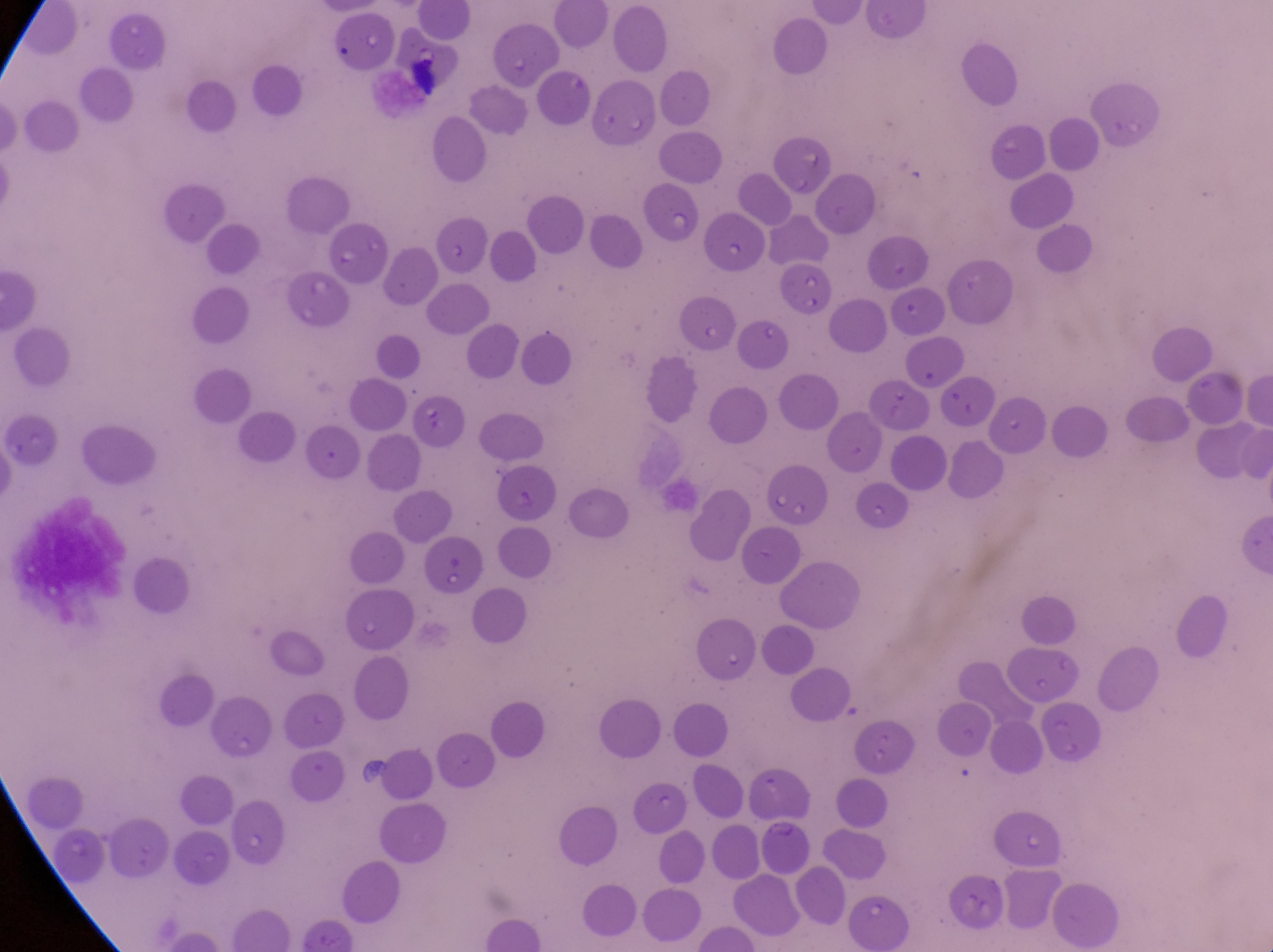
{
  "preparation": "thin blood smear",
  "capture": "smartphone photograph through the eyepiece of an Olympus CX-23 microscope",
  "parasitised_red_blood_cell_locations": "approximate bounding boxes as [left, top, right, bottom] in pixels: [639, 180, 701, 250], [329, 218, 392, 278], [435, 218, 490, 275]",
  "field_of_view": "single",
  "country": "Uganda",
  "image_size": "1273×952 pixels",
  "magnification": "1000x"
}